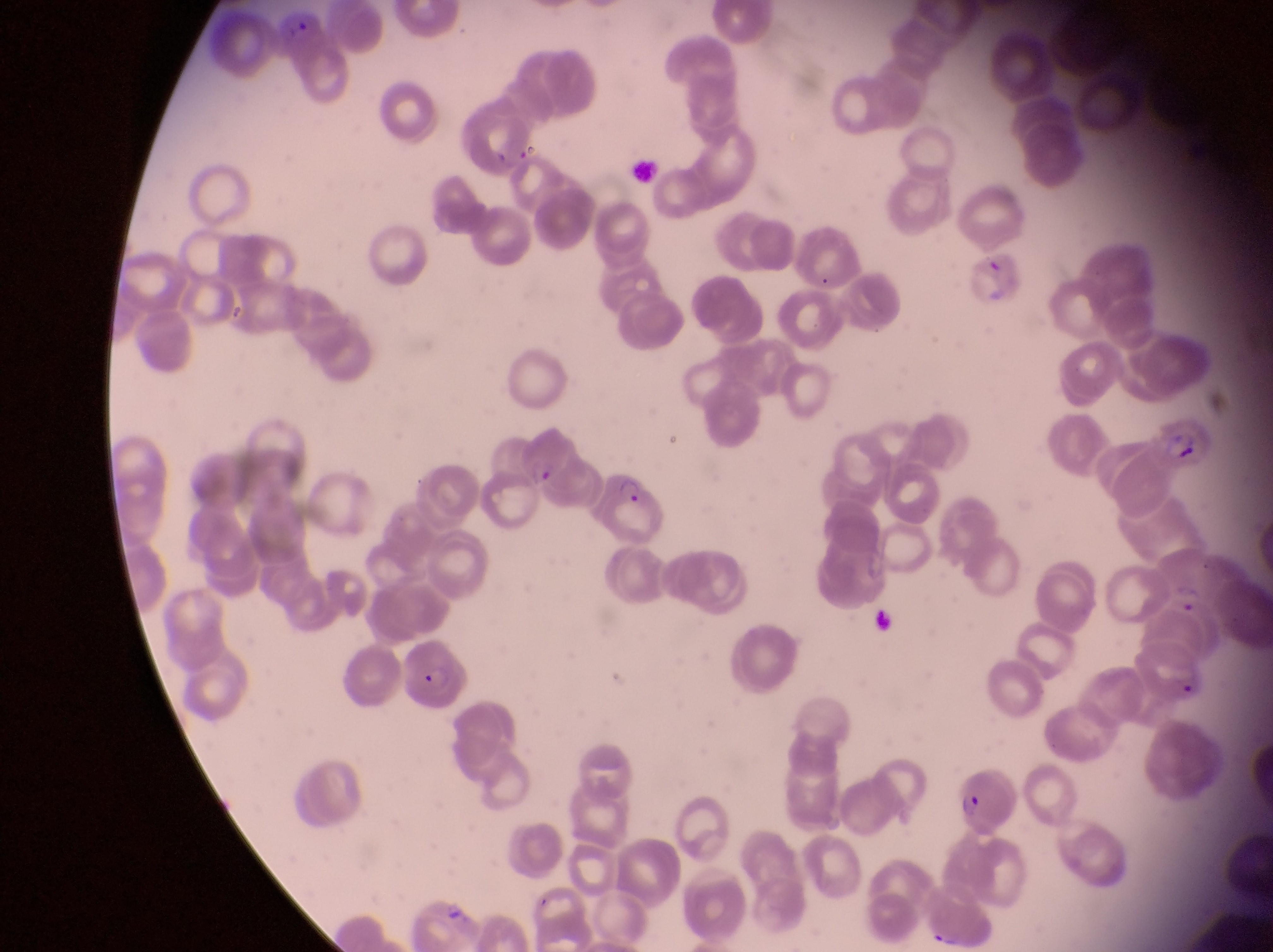 Approximate bounding boxes as [left, top, right, bottom] in pixels. Parasitised red blood cell locations: [969, 252, 1021, 303], [1151, 409, 1213, 471], [507, 434, 582, 494], [587, 470, 667, 544], [1148, 554, 1226, 617], [1131, 640, 1208, 710], [394, 652, 474, 709], [948, 777, 1015, 839]. Artifact (platelet-like body, stain precipitate, or debris) locations: [630, 154, 663, 182]. Single field of view. Sample from Uganda. Image is 1273×952 pixels. Thin blood smear. Photographed through the eyepiece of an Olympus CX-23 microscope with a smartphone camera. At a magnification of 1000x.